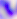 400x magnification. Toxoplasma gondii is shown. Photomicrograph.